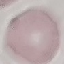

Malaria status: uninfected. Acquired by smartphone through the microscope eyepiece. Cell patch, automatically extracted from a larger field of view and resized to 64 × 64 pixels. Giemsa-stained preparation. Thin smear of blood.